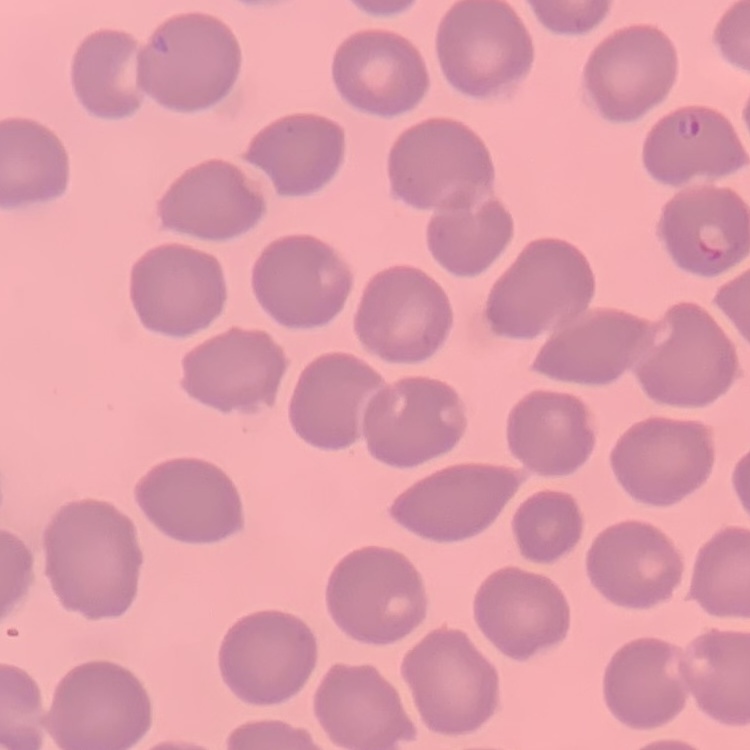
Summary:
  - Red blood cell morphology: no rouleaux formation
  - Image type: square crop of a larger photomicrograph
  - Stain: Field's or Giemsa
  - Preparation: thin blood film